State which parasite is depicted.
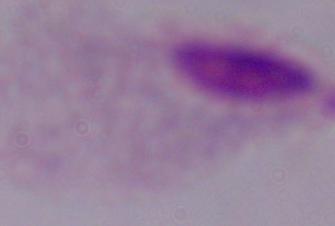

This is a trichomonad.

Summary:
  - Magnification: 1000x
  - Modality: photomicrograph